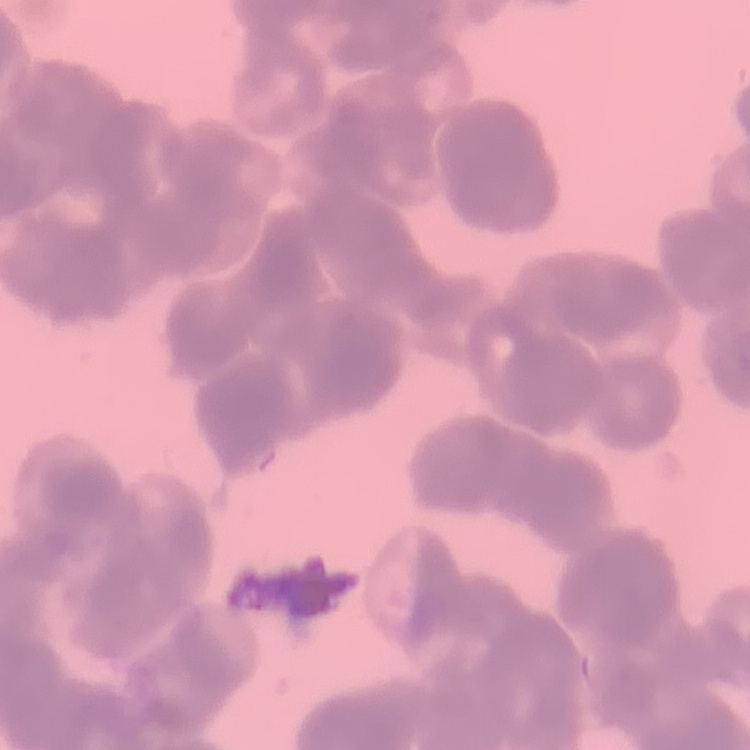

The red blood cells show rouleaux formation. One tile cut from a larger photomicrograph. Field's or Giemsa stain. Thin blood smear.